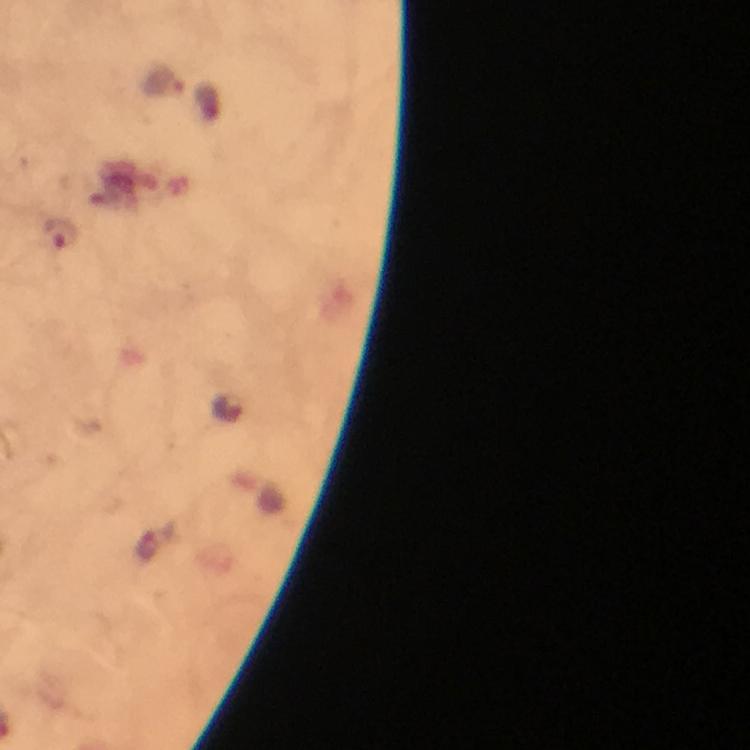
Approximate centers as [x, y] in pixels. Plasmodium parasite locations: [165, 82], [59, 233]. At 100x magnification. Photographed through the microscope with a smartphone camera. Immersion oil was used. From a malaria diagnostic workup. Image is 750×750 pixels. Thick blood smear. A crop from one field of view. Giemsa-stained preparation.